Assess the morphology of the erythrocytes.
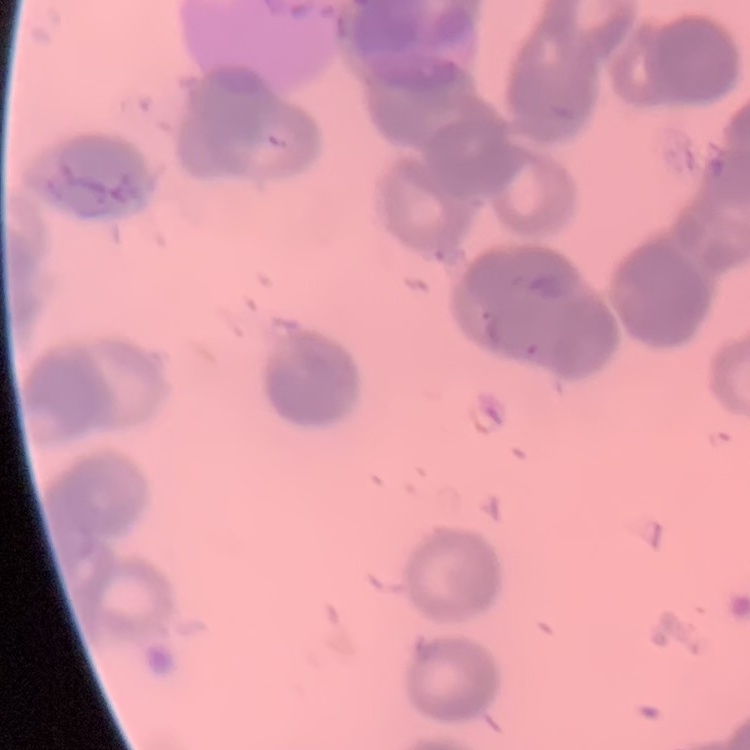

They show rouleaux formation.

image type = one tile cut from a larger photomicrograph
preparation = thin blood film
stain = Field's or Giemsa